Classify this cell by malaria status.
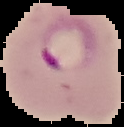

Parasitized.

preparation = thin blood smear
image size = 124×127 pixels
image type = cell region segmented out of the field of view; surrounding area masked to black